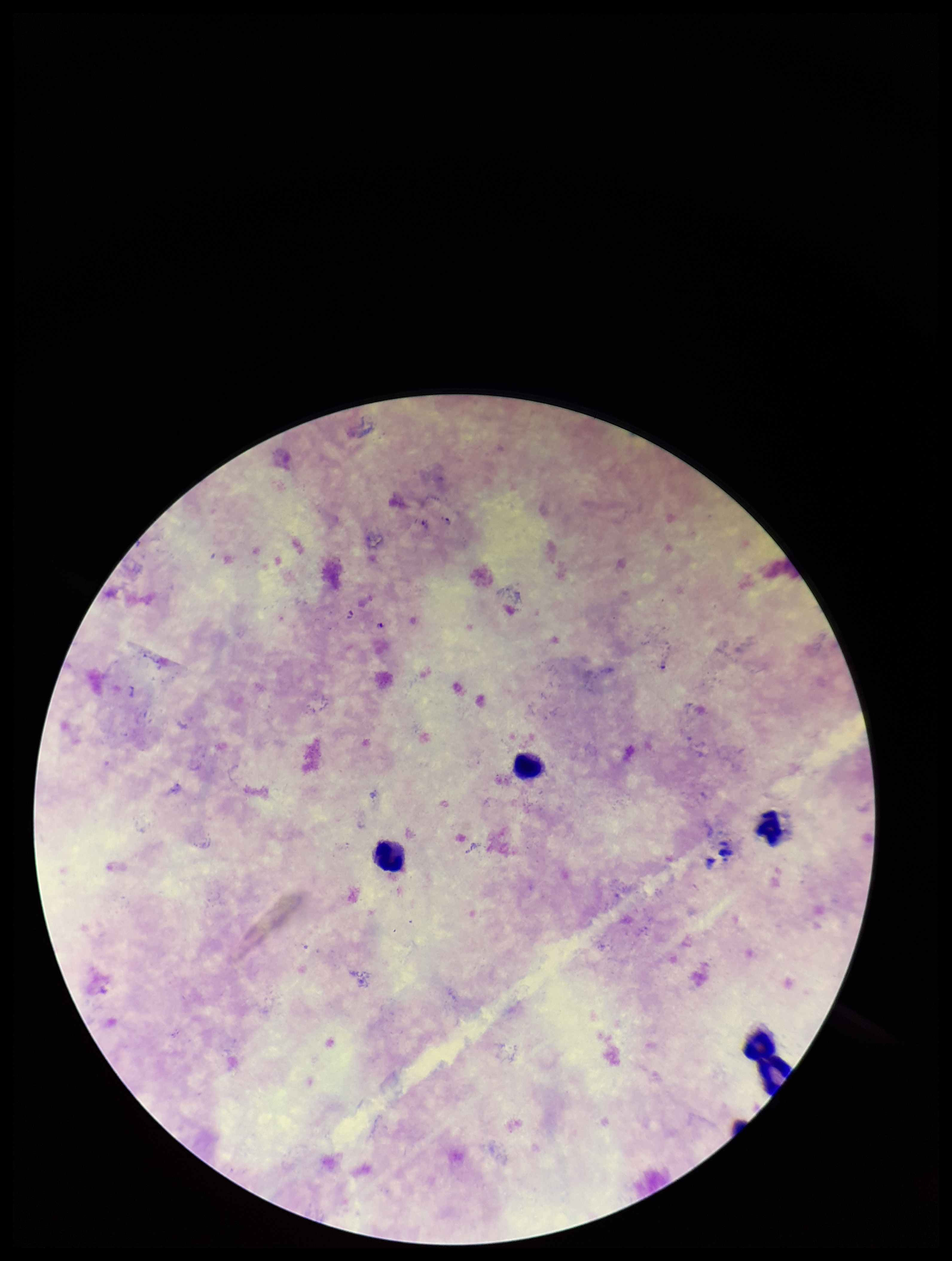
Summary:
  - Field of view: single
  - Leukocyte count: 3
  - Preparation: thick smear
  - Capture: smartphone photograph through the microscope eyepiece
  - Parasite count: 3
  - Species reported for this patient: Plasmodium falciparum
  - Image size: 952×1261 pixels
  - Patient malaria status: positive
  - Plasmodium parasites: seen
  - Stain: Giemsa